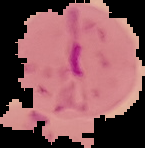

{
  "image_size": "145×148 pixels",
  "result": "malaria parasites detected",
  "image_type": "cell region segmented out of the field of view; surrounding area masked to black",
  "preparation": "thin blood smear"
}